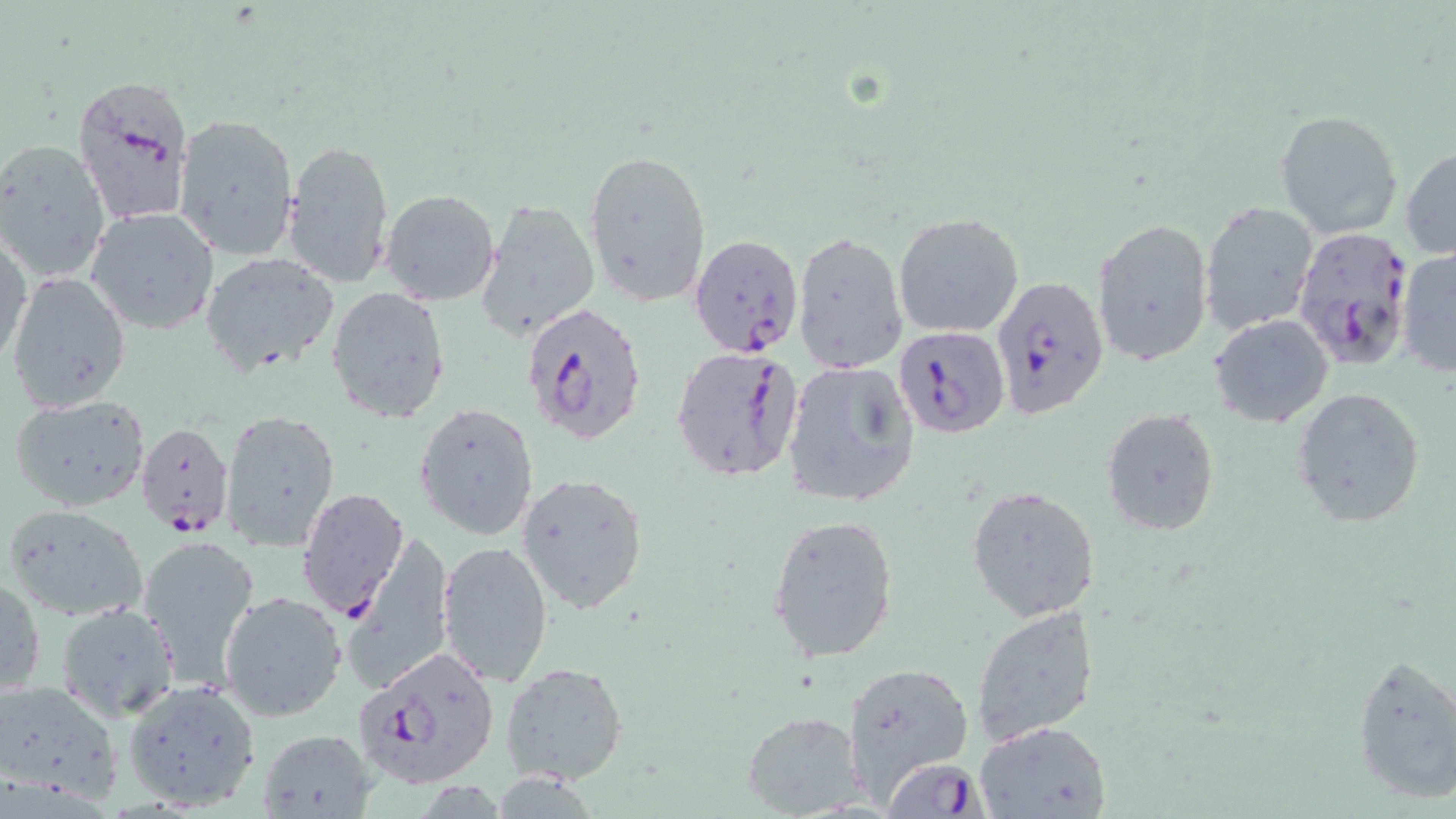

Approximate bounding boxes as named x1/y1/x2/y2 corners in pixels. Uninfected red blood cell locations: (x1=1274, y1=108, x2=1403, y2=241), (x1=174, y1=113, x2=299, y2=261), (x1=1, y1=138, x2=113, y2=286), (x1=284, y1=139, x2=396, y2=288), (x1=1401, y1=145, x2=1456, y2=260), (x1=582, y1=147, x2=711, y2=309), (x1=380, y1=190, x2=500, y2=306), (x1=478, y1=198, x2=600, y2=343), (x1=1200, y1=200, x2=1319, y2=335), (x1=87, y1=207, x2=218, y2=335), (x1=893, y1=212, x2=1024, y2=338), (x1=1093, y1=216, x2=1214, y2=367), (x1=1, y1=229, x2=31, y2=366), (x1=792, y1=230, x2=906, y2=373), (x1=1396, y1=247, x2=1456, y2=378), (x1=201, y1=252, x2=338, y2=374), (x1=7, y1=272, x2=131, y2=415), (x1=327, y1=288, x2=452, y2=424), (x1=1210, y1=313, x2=1334, y2=425), (x1=782, y1=361, x2=920, y2=507), (x1=1290, y1=386, x2=1428, y2=530), (x1=9, y1=396, x2=152, y2=513), (x1=413, y1=402, x2=541, y2=541), (x1=1101, y1=407, x2=1219, y2=537), (x1=222, y1=409, x2=340, y2=551), (x1=516, y1=472, x2=651, y2=618), (x1=966, y1=485, x2=1097, y2=622), (x1=4, y1=502, x2=150, y2=621), (x1=767, y1=512, x2=900, y2=663), (x1=343, y1=530, x2=454, y2=692), (x1=136, y1=534, x2=260, y2=685), (x1=439, y1=541, x2=554, y2=686), (x1=0, y1=574, x2=45, y2=699), (x1=220, y1=591, x2=348, y2=723), (x1=58, y1=603, x2=181, y2=720), (x1=970, y1=605, x2=1097, y2=746), (x1=1351, y1=653, x2=1456, y2=805), (x1=840, y1=660, x2=973, y2=801), (x1=501, y1=661, x2=628, y2=786), (x1=121, y1=679, x2=263, y2=813), (x1=0, y1=680, x2=123, y2=804), (x1=740, y1=711, x2=866, y2=818), (x1=973, y1=720, x2=1113, y2=818), (x1=256, y1=727, x2=378, y2=819). Plasmodium falciparum-infected red blood cell locations: (x1=72, y1=73, x2=196, y2=229), (x1=1291, y1=223, x2=1419, y2=372), (x1=688, y1=234, x2=806, y2=357), (x1=990, y1=276, x2=1109, y2=421), (x1=521, y1=299, x2=649, y2=449), (x1=893, y1=325, x2=1011, y2=437), (x1=669, y1=346, x2=803, y2=483), (x1=136, y1=420, x2=234, y2=537), (x1=296, y1=488, x2=409, y2=619), (x1=351, y1=647, x2=501, y2=790), (x1=873, y1=760, x2=980, y2=819). Slide-level diagnosis: Plasmodium falciparum. Light microscopy. May-Grünwald-Giemsa stain. Thin blood smear. Image is 1456×819 pixels. Single field of view. 1000x magnification.